Locate Plasmodium parasites and leukocytes.
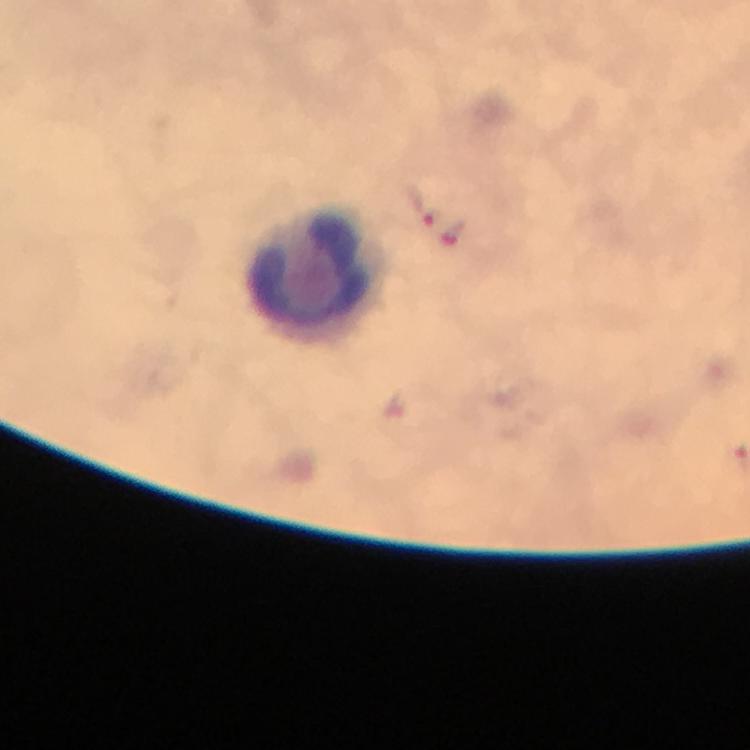

Approximate centers as (x, y) in pixels.
Plasmodium parasites: (420, 205), (455, 237).
Leukocytes: (321, 271).

Giemsa stain. 100x magnification. Image is 750×750 pixels. Immersion oil applied. From a malaria diagnostic workup. A crop from one field of view. Photographed with a smartphone mounted on the microscope. Thick smear.